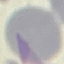

Result: no malaria parasites detected. Giemsa stain. Automatically extracted cell patch, resized to 64 × 64 pixels. Acquired by smartphone through the microscope eyepiece. Thin blood film.